Locate every Plasmodium parasite and every leukocyte.
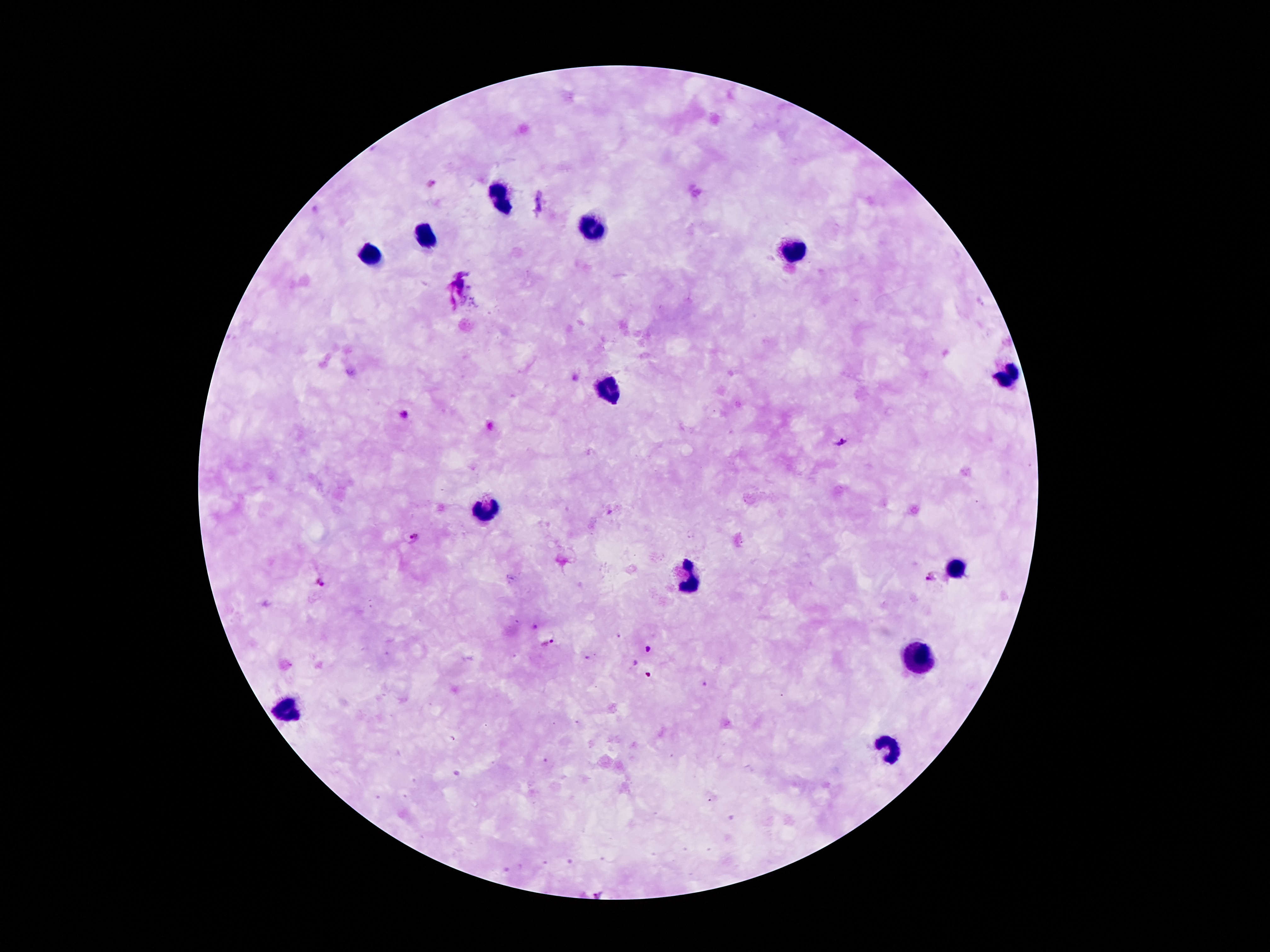

Approximate centers as {x, y} in pixels.
Plasmodium parasites: {404, 415}, {841, 441}, {416, 540}, {931, 578}, {320, 581}, {548, 643}, {648, 650}.
Leukocytes: {500, 200}, {592, 228}, {424, 235}, {793, 251}, {371, 253}, {1007, 375}, {607, 391}, {487, 509}, {959, 566}, {689, 581}, {915, 653}, {283, 711}, {886, 750}.

magnification = 100x
image size = 1270×952 pixels
capture = smartphone camera through the microscope eyepiece
field of view = single
patient malaria status = positive for Plasmodium falciparum
preparation = thick peripheral-blood smear
stain = Giemsa